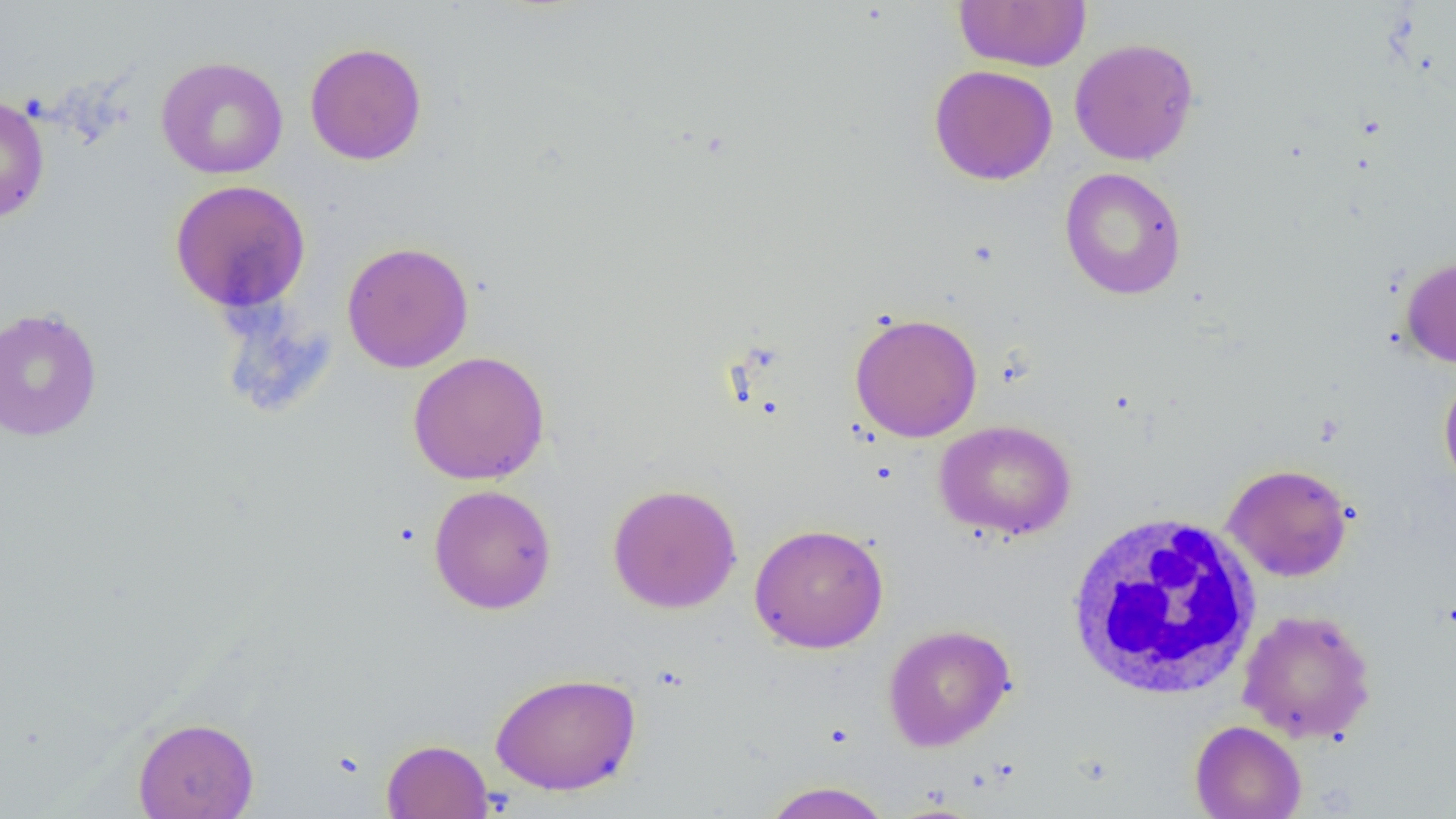
Summary:
  - Coordinate format: approximate bounding boxes as named x1/y1/x2/y2 corners in pixels
  - White blood cell locations: (x1=1064, y1=511, x2=1265, y2=701)
  - Uninfected red blood cell locations: (x1=954, y1=0, x2=1091, y2=72), (x1=1069, y1=37, x2=1199, y2=166), (x1=304, y1=42, x2=428, y2=165), (x1=156, y1=56, x2=288, y2=179), (x1=928, y1=64, x2=1058, y2=186), (x1=0, y1=93, x2=50, y2=225), (x1=1059, y1=167, x2=1187, y2=300), (x1=169, y1=179, x2=311, y2=315), (x1=341, y1=241, x2=475, y2=373), (x1=1400, y1=255, x2=1456, y2=368), (x1=0, y1=306, x2=103, y2=442), (x1=849, y1=312, x2=983, y2=442), (x1=407, y1=350, x2=550, y2=485), (x1=1438, y1=367, x2=1456, y2=496), (x1=934, y1=420, x2=1077, y2=540), (x1=1222, y1=463, x2=1354, y2=582), (x1=607, y1=483, x2=742, y2=614), (x1=428, y1=484, x2=557, y2=615), (x1=748, y1=523, x2=889, y2=653), (x1=1237, y1=608, x2=1377, y2=744), (x1=883, y1=624, x2=1016, y2=751), (x1=489, y1=671, x2=642, y2=796), (x1=132, y1=716, x2=259, y2=819), (x1=1189, y1=719, x2=1307, y2=819), (x1=381, y1=739, x2=494, y2=819), (x1=760, y1=781, x2=894, y2=819)
  - Slide-level diagnosis: negative for blood parasites
  - Magnification: 1000x
  - Field of view: one of a larger specimen
  - Image size: 1456×819 pixels
  - Preparation: thin blood smear
  - Modality: light microscopy